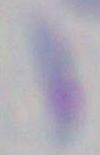

Summary:
  - Identification: Toxoplasma gondii
  - Magnification: 1000x
  - Modality: photomicrograph